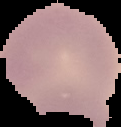

Summary:
  - Image size: 121×127 pixels
  - Malaria status: uninfected
  - Preparation: thin blood film
  - Image type: segmented cell region with the area outside set to black